Identify the parasite.
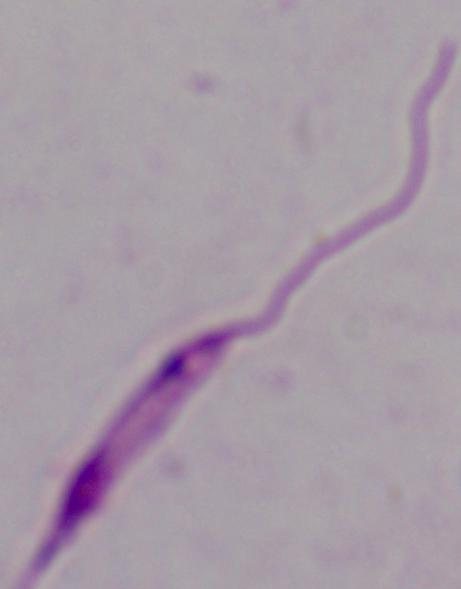

Leishmania.

Summary:
  - Magnification: 1000x
  - Modality: photomicrograph